Classify this cell by malaria status.
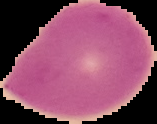

Uninfected.

Summary:
  - Preparation: thin blood film
  - Image size: 157×124 pixels
  - Image type: cell region segmented out of the field of view; surrounding area masked to black